Comment on the morphology of the red blood cells.
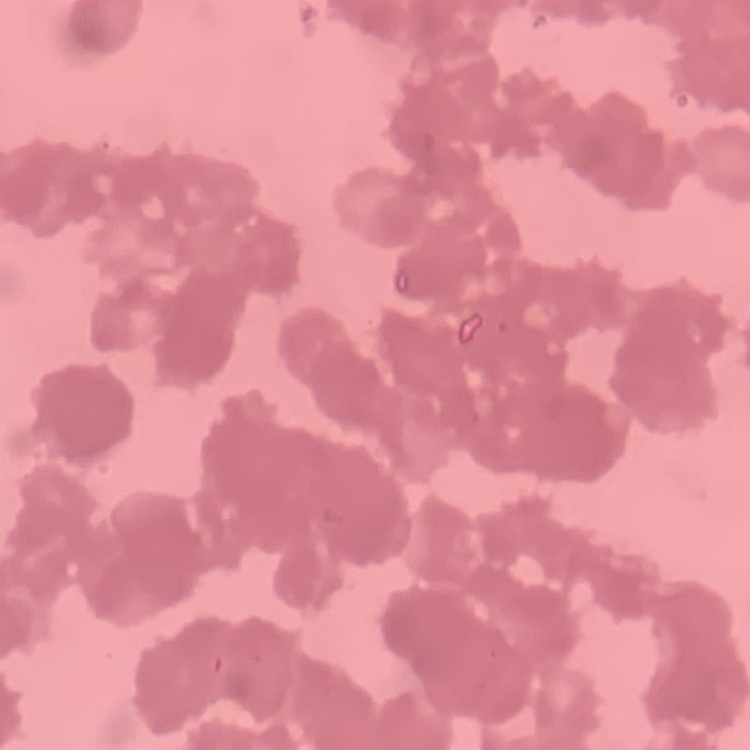

Rouleaux formation.

Summary:
  - Image type: one tile cut from a larger photomicrograph
  - Stain: Field's or Giemsa
  - Preparation: thin blood film